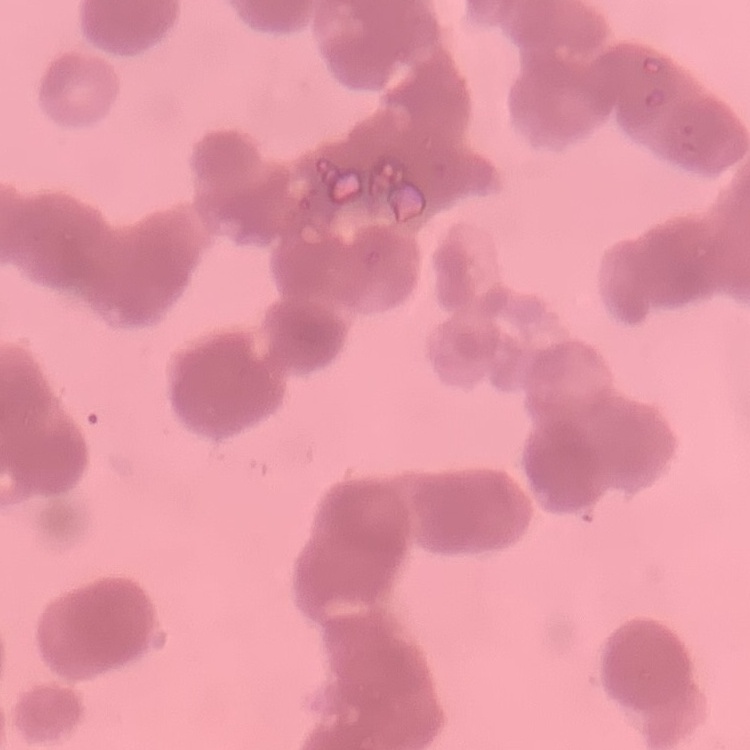
The erythrocytes exhibit rouleaux formation. Stained with either Field's or Giemsa. Thin blood film. One tile cut from a larger photomicrograph.